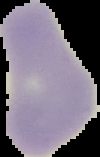

From a thin blood smear. Result: no malaria parasites seen. The area outside the segmented cell region is set to black. Image is 100×157 pixels.